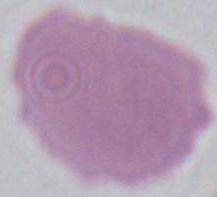
{
  "magnification": "1000x",
  "modality": "photomicrograph",
  "identification": "erythrocyte"
}